State which parasite is depicted.
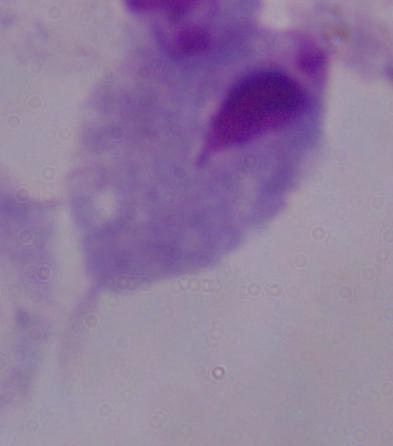

This is a trichomonad.

magnification: 1000x
modality: micrograph